Outline each blood parasite and name the species.
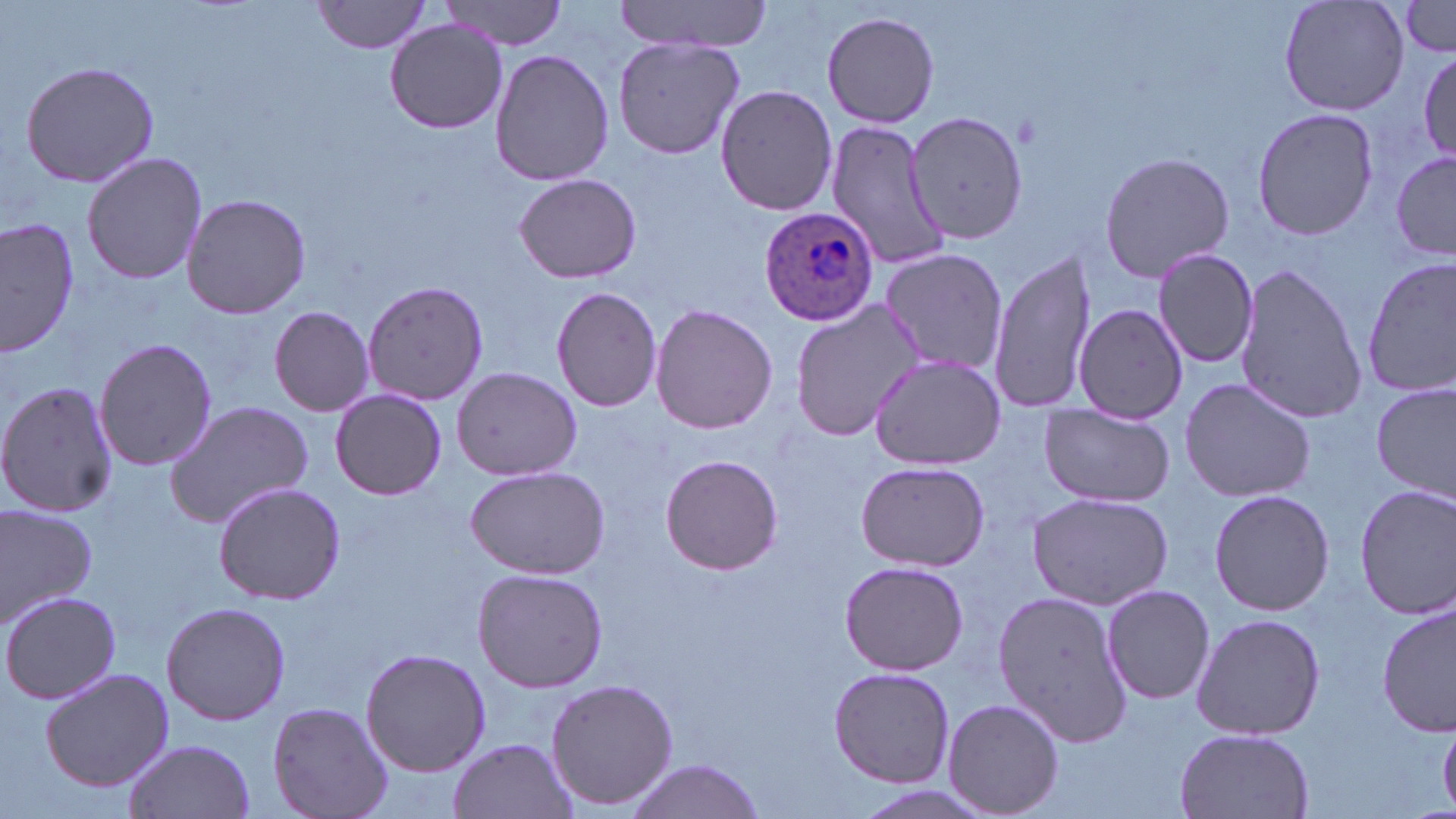
Approximate bounding boxes as (x1, y1, x2, y2) in pixels.
Plasmodium ovale-infected red blood cells: (760, 206, 880, 325).
No Plasmodium falciparum, Plasmodium malariae, Plasmodium vivax, Babesia divergens, or Trypanosoma brucei observed.

{
  "slide_level_diagnosis": "Plasmodium ovale",
  "modality": "light microscopy",
  "magnification": "1000x",
  "image_size": "1456×819 pixels",
  "uninfected_red_blood_cell_locations": "approximate bounding boxes as (x1, y1, x2, y2) in pixels: (613, 0, 775, 54), (1279, 0, 1410, 116), (313, 1, 437, 55), (441, 1, 570, 51), (1397, 1, 1456, 62), (822, 10, 942, 127), (384, 17, 509, 133), (612, 34, 744, 161), (1417, 49, 1456, 163), (489, 51, 616, 187), (20, 60, 161, 189), (715, 85, 839, 215), (1251, 106, 1382, 243), (907, 109, 1029, 249), (822, 116, 954, 272), (1390, 147, 1454, 264), (81, 150, 208, 285), (1097, 150, 1236, 283), (512, 172, 643, 284), (181, 193, 311, 318), (2, 217, 81, 358), (879, 247, 1009, 377), (989, 247, 1100, 414), (1153, 248, 1261, 368), (1360, 255, 1455, 398), (1233, 262, 1366, 428), (362, 280, 488, 406), (551, 286, 663, 413), (790, 299, 923, 442), (1073, 304, 1187, 424), (649, 305, 778, 434), (268, 306, 374, 417), (94, 337, 218, 471), (869, 355, 1004, 469), (451, 366, 582, 481), (1177, 377, 1316, 501), (0, 380, 119, 520), (1373, 383, 1454, 502), (329, 389, 446, 499), (164, 401, 315, 529), (1038, 404, 1173, 507), (659, 454, 783, 574), (854, 460, 990, 571), (464, 465, 609, 579), (212, 481, 346, 605), (1352, 484, 1456, 617), (1207, 489, 1335, 616), (1027, 492, 1173, 610), (0, 504, 99, 628), (838, 558, 969, 676), (472, 567, 608, 692), (1100, 583, 1215, 705), (991, 590, 1136, 750), (2, 591, 121, 705), (161, 601, 291, 725), (1378, 604, 1453, 738), (1191, 611, 1326, 741), (16, 625, 152, 764), (359, 647, 491, 777), (828, 666, 955, 788), (40, 667, 175, 791), (545, 677, 678, 811), (944, 697, 1064, 817), (268, 702, 392, 819), (1439, 720, 1456, 812), (1174, 728, 1316, 819), (448, 736, 579, 818), (121, 739, 256, 819), (619, 759, 771, 818)",
  "field_of_view": "one of a larger specimen",
  "stain": "May-Grünwald-Giemsa",
  "preparation": "thin blood film"
}